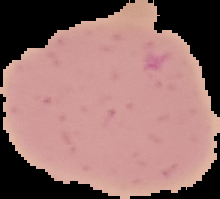

{
  "image_size": "220×199 pixels",
  "result": "no malaria parasites seen",
  "preparation": "thin blood film",
  "image_type": "segmented cell region with the area outside set to black"
}